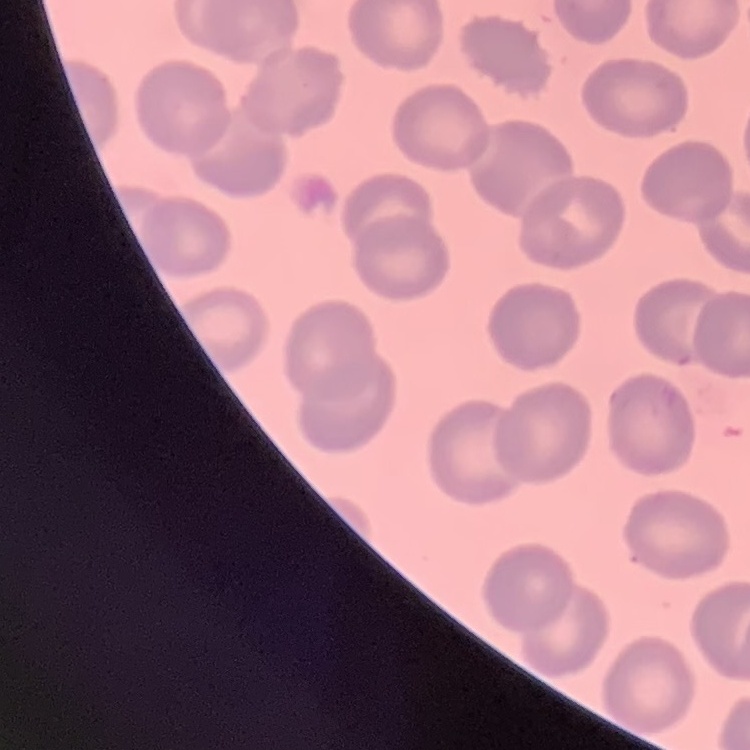
red blood cell morphology = no rouleaux formation
preparation = thin peripheral smear
stain = Field's or Giemsa
image type = square crop of a larger photomicrograph